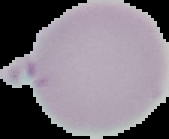
image_type: cell region segmented out of the field of view; surrounding area masked to black
preparation: thin blood film
image_size: 169×139 pixels
malaria_status: uninfected